Comment on the morphology of the red blood cells.
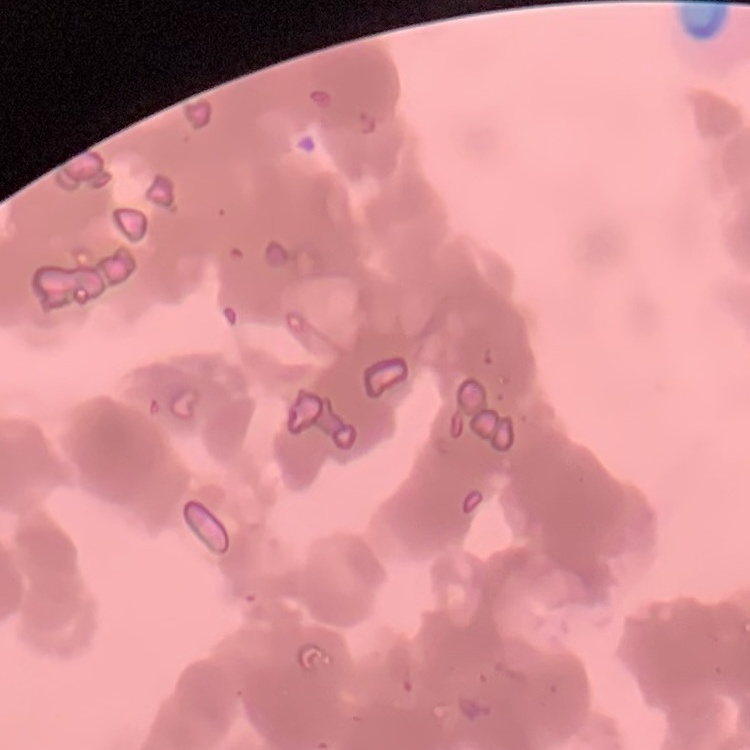

They show rouleaux formation.

preparation = thin blood smear
stain = Field's or Giemsa
image type = one tile cut from a larger photomicrograph